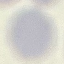
Summary:
  - Malaria status: uninfected
  - Image type: automatically extracted cell patch, resized to 64 × 64 pixels
  - Stain: Giemsa
  - Capture: smartphone through the microscope eyepiece
  - Preparation: thin blood film